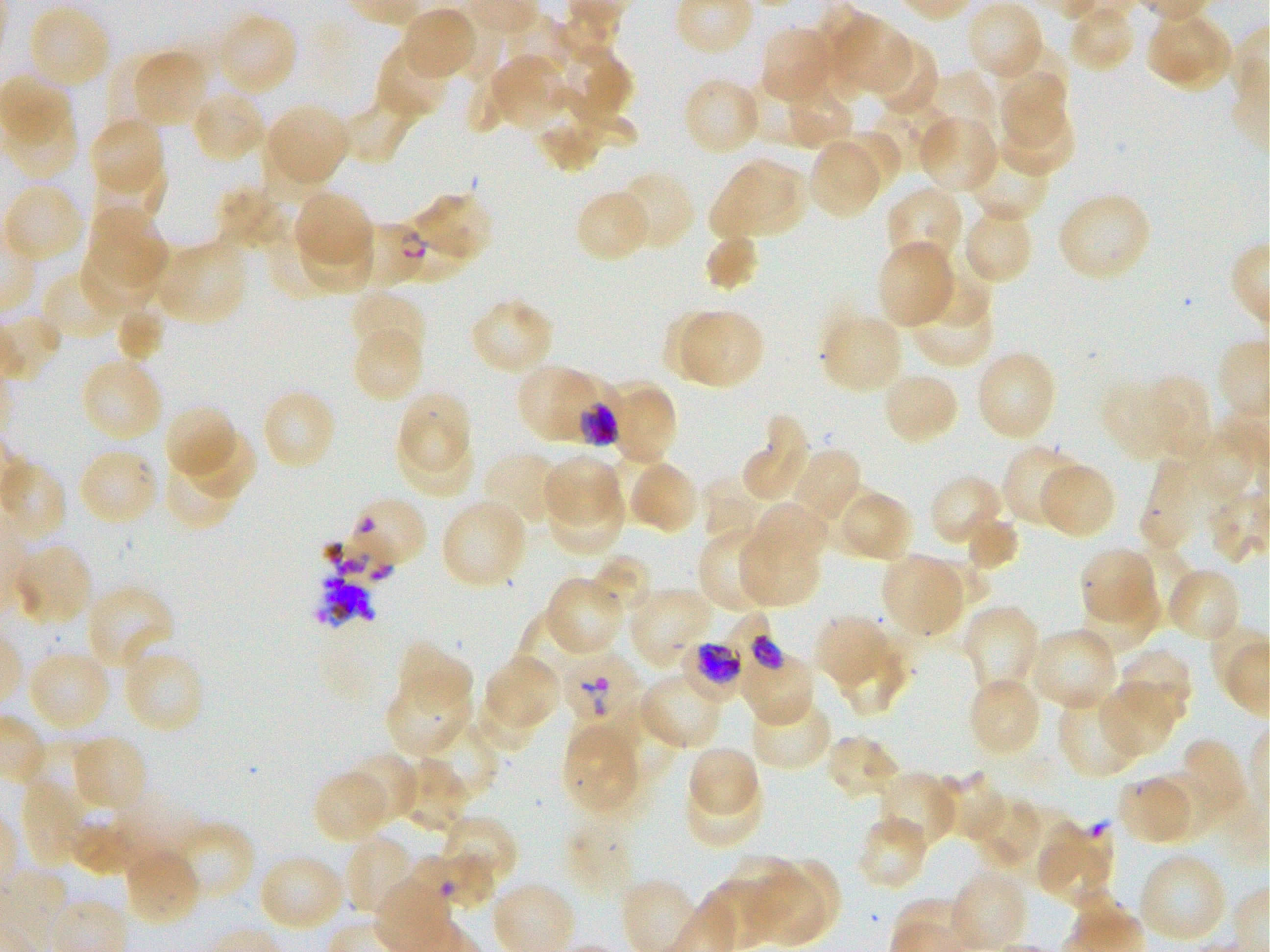

Approximate bounding boxes as [x1, y1, x2, y2] in pixels. Not every red blood cell is marked. A life-cycle stage — or a range of stages, where the recorded stages span more than one — follows each staged infected red blood cell.
Summary:
  - Locations of infected red blood cells: [353, 221, 426, 289] ring; [738, 636, 816, 728] trophozoite; [679, 639, 746, 703] trophozoite; [559, 649, 639, 732] early ring to early trophozoite
  - Locations of uninfected red blood cells: [967, 2, 1044, 82], [1067, 4, 1134, 74], [27, 5, 111, 90], [400, 6, 478, 80], [215, 12, 299, 96], [502, 13, 570, 88], [831, 15, 910, 95], [1148, 15, 1232, 92], [758, 24, 835, 104], [867, 37, 939, 118], [995, 41, 1070, 113], [375, 42, 451, 121], [563, 49, 633, 122], [133, 50, 207, 128], [106, 56, 174, 132], [490, 56, 565, 129], [464, 72, 510, 137], [931, 72, 1000, 146], [1001, 72, 1068, 147], [681, 76, 762, 156], [740, 78, 817, 149], [782, 83, 854, 150], [555, 86, 637, 149], [191, 89, 267, 164], [338, 90, 421, 166], [873, 95, 960, 171], [265, 103, 350, 187], [999, 103, 1075, 177], [6, 107, 79, 180], [537, 110, 605, 173], [919, 116, 998, 193], [88, 117, 165, 196], [257, 127, 334, 200], [830, 128, 900, 193], [808, 139, 882, 218], [966, 144, 1052, 223], [711, 160, 806, 239], [92, 165, 167, 235], [617, 170, 696, 252], [5, 184, 84, 264], [885, 185, 964, 269], [214, 187, 289, 252], [573, 189, 652, 263], [293, 190, 372, 269], [1056, 190, 1152, 283], [409, 191, 494, 264], [88, 203, 169, 288], [961, 206, 1035, 286], [295, 220, 375, 293], [270, 225, 347, 301], [703, 235, 759, 291], [80, 239, 158, 314], [155, 241, 248, 326], [876, 241, 955, 330], [43, 270, 125, 341], [922, 271, 988, 330], [908, 283, 994, 369], [348, 289, 427, 363], [469, 297, 557, 376], [115, 304, 167, 364], [662, 310, 731, 381], [677, 310, 762, 388], [822, 314, 902, 393], [351, 328, 425, 403], [975, 350, 1058, 441], [79, 357, 164, 442], [517, 364, 611, 444], [881, 370, 960, 447], [1146, 373, 1211, 458], [605, 379, 678, 467], [1099, 379, 1175, 462], [261, 388, 338, 471], [397, 391, 472, 471], [164, 403, 236, 482], [740, 414, 811, 503], [184, 426, 258, 500], [398, 428, 475, 499], [1193, 430, 1255, 498], [1002, 443, 1086, 530], [601, 446, 672, 522], [78, 449, 160, 525], [791, 449, 863, 526], [163, 451, 239, 530], [482, 451, 560, 527], [543, 454, 622, 525], [1141, 458, 1219, 552], [628, 460, 699, 535], [1039, 461, 1116, 538], [929, 474, 1004, 549], [702, 476, 768, 542], [814, 484, 890, 558], [546, 487, 624, 556], [843, 489, 913, 561], [440, 498, 528, 589], [752, 502, 828, 571], [965, 513, 1019, 573], [697, 530, 774, 614], [737, 530, 820, 608], [14, 544, 93, 626], [1079, 546, 1158, 623], [1122, 546, 1197, 628], [586, 554, 651, 620], [880, 554, 964, 635], [921, 559, 991, 622], [1166, 567, 1242, 643], [545, 576, 623, 657], [86, 584, 175, 672], [1080, 586, 1158, 655], [629, 588, 714, 667], [962, 603, 1041, 701], [512, 611, 586, 693], [815, 615, 888, 688], [1028, 627, 1119, 713], [841, 637, 912, 717], [395, 641, 473, 712], [122, 645, 206, 735], [27, 649, 111, 732], [1117, 649, 1194, 727], [484, 654, 561, 730], [637, 673, 725, 751], [966, 676, 1041, 758], [385, 678, 472, 757], [1097, 683, 1173, 758], [472, 695, 539, 755], [750, 696, 834, 771], [1058, 698, 1141, 779], [422, 719, 499, 802], [562, 722, 639, 813], [70, 734, 147, 812], [825, 734, 902, 802], [1182, 738, 1247, 816], [687, 744, 760, 817], [16, 745, 105, 816], [346, 752, 419, 826], [397, 758, 467, 834], [312, 769, 391, 844], [932, 770, 1005, 844], [876, 771, 958, 852], [1149, 771, 1221, 837], [684, 776, 762, 849], [1116, 776, 1193, 845], [19, 778, 87, 868], [973, 798, 1044, 873], [67, 804, 137, 876], [441, 814, 519, 891], [565, 815, 636, 900], [856, 815, 929, 892], [173, 820, 256, 905], [1036, 824, 1113, 904], [343, 835, 415, 918], [122, 845, 201, 928], [1138, 851, 1228, 946], [258, 854, 347, 933], [725, 855, 805, 930], [763, 857, 840, 931], [748, 872, 824, 944], [951, 872, 1027, 950]
  - Locations of red blood cells of indeterminate infection status: [393, 211, 469, 283], [346, 495, 428, 570], [414, 851, 506, 913]
  - Life-cycle stages observed: ring, trophozoite
  - Stain: Giemsa
  - Preparation: thin blood smear
  - Field of view: one from this slide
  - Donor blood group: O+
  - Culture: in-vitro Plasmodium falciparum strain 3D7, static
  - Objective: 100x, oil immersion, numerical aperture 1.25
  - Image size: 1270×952 pixels